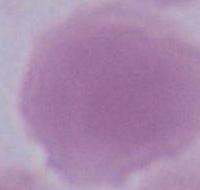

Summary:
  - Magnification: 1000x
  - Modality: photomicrograph
  - Identification: red blood cell